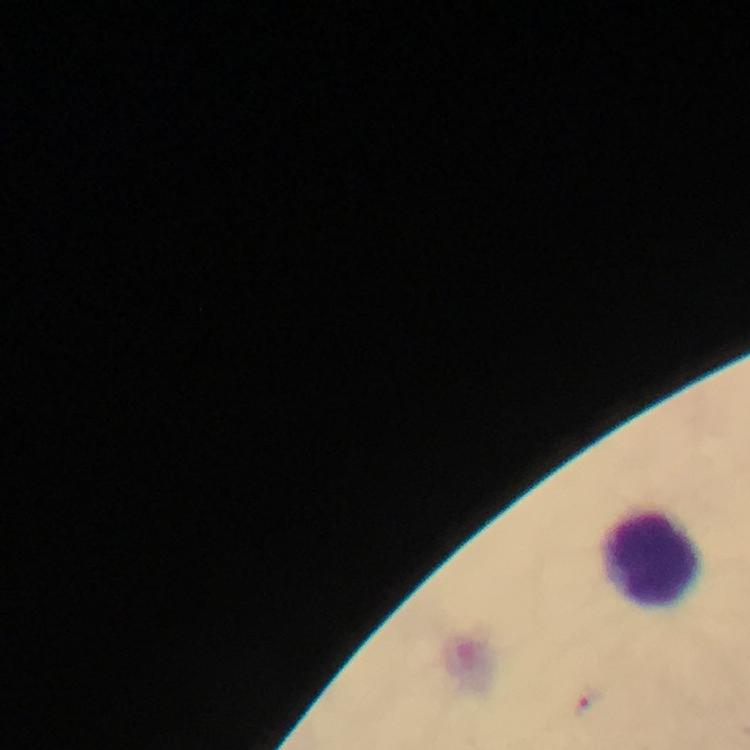

context = from a malaria diagnostic workup
malaria parasite locations = approximate centers as [x, y] in pixels: [586, 705]
leukocyte locations = approximate centers as [x, y] in pixels: [658, 564]
stain = Giemsa
magnification = 100x
cropped from = a single field of view
immersion oil = used
capture = smartphone mounted on the microscope
preparation = thick smear
image size = 750×750 pixels